Outline each uninfected red blood cell.
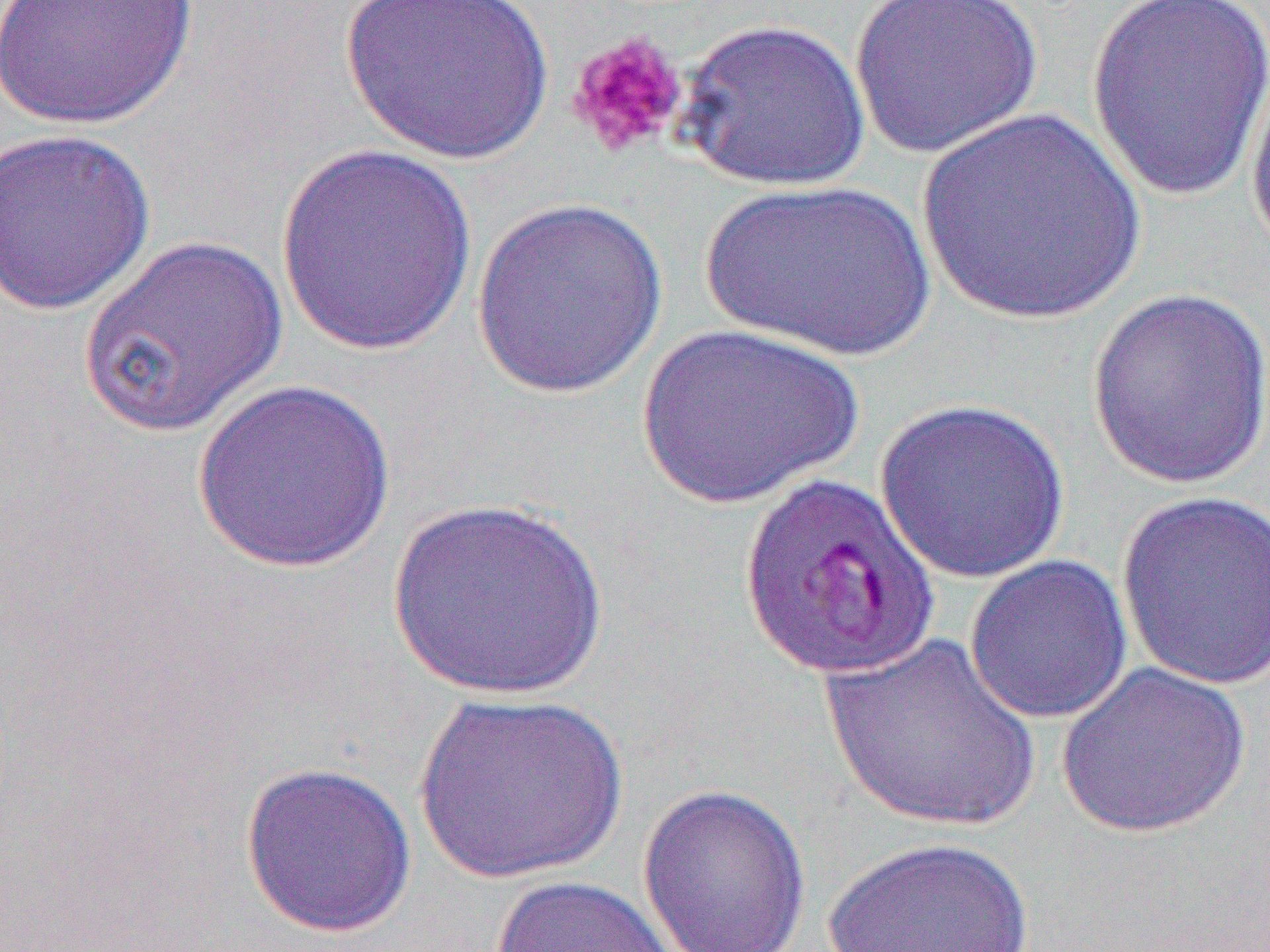

Approximate bounding boxes as (x1,y1)-(x2,y2) corner pairs in pixels.
Uninfected red blood cells: (1,0)-(200,132), (340,0)-(555,166), (849,0)-(1044,160), (1085,2)-(1270,205), (676,18)-(872,193), (1245,61)-(1270,262), (916,108)-(1147,328), (1,127)-(156,316), (274,145)-(479,357), (697,178)-(938,363), (471,196)-(669,399), (77,235)-(287,439), (1087,288)-(1270,490), (636,322)-(864,510), (191,379)-(397,573), (874,396)-(1071,584), (1115,491)-(1270,692), (388,497)-(610,700), (964,554)-(1135,725), (819,631)-(1044,834), (1056,660)-(1251,839), (412,691)-(629,885), (239,761)-(417,938), (637,783)-(811,952), (820,836)-(1037,952), (488,874)-(684,952).

Platelet locations: (565,30)-(691,160). Slide-level diagnosis: Plasmodium falciparum. Captured at 1000x magnification. Light microscopy. Image is 1270×952 pixels. One field of a larger specimen. Thin blood film.